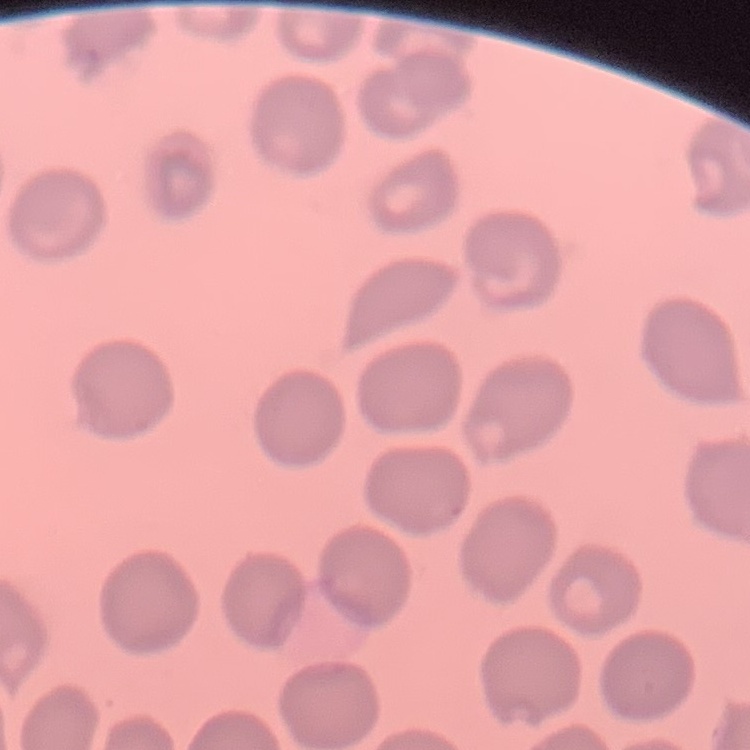
{
  "red_blood_cell_morphology": "no rouleaux formation",
  "image_type": "square crop of a larger photomicrograph",
  "stain": "Field's or Giemsa",
  "preparation": "thin blood film"
}